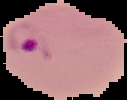

result = malaria parasites detected
image type = segmented cell region with the area outside set to black
image size = 127×100 pixels
preparation = thin blood smear